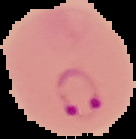
Summary:
  - Image type: cell region segmented out of the field of view; surrounding area masked to black
  - Preparation: thin blood smear
  - Malaria status: parasitized
  - Image size: 136×139 pixels